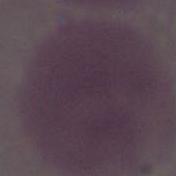

An erythrocyte is seen. Captured at 1000x magnification. Photomicrograph.